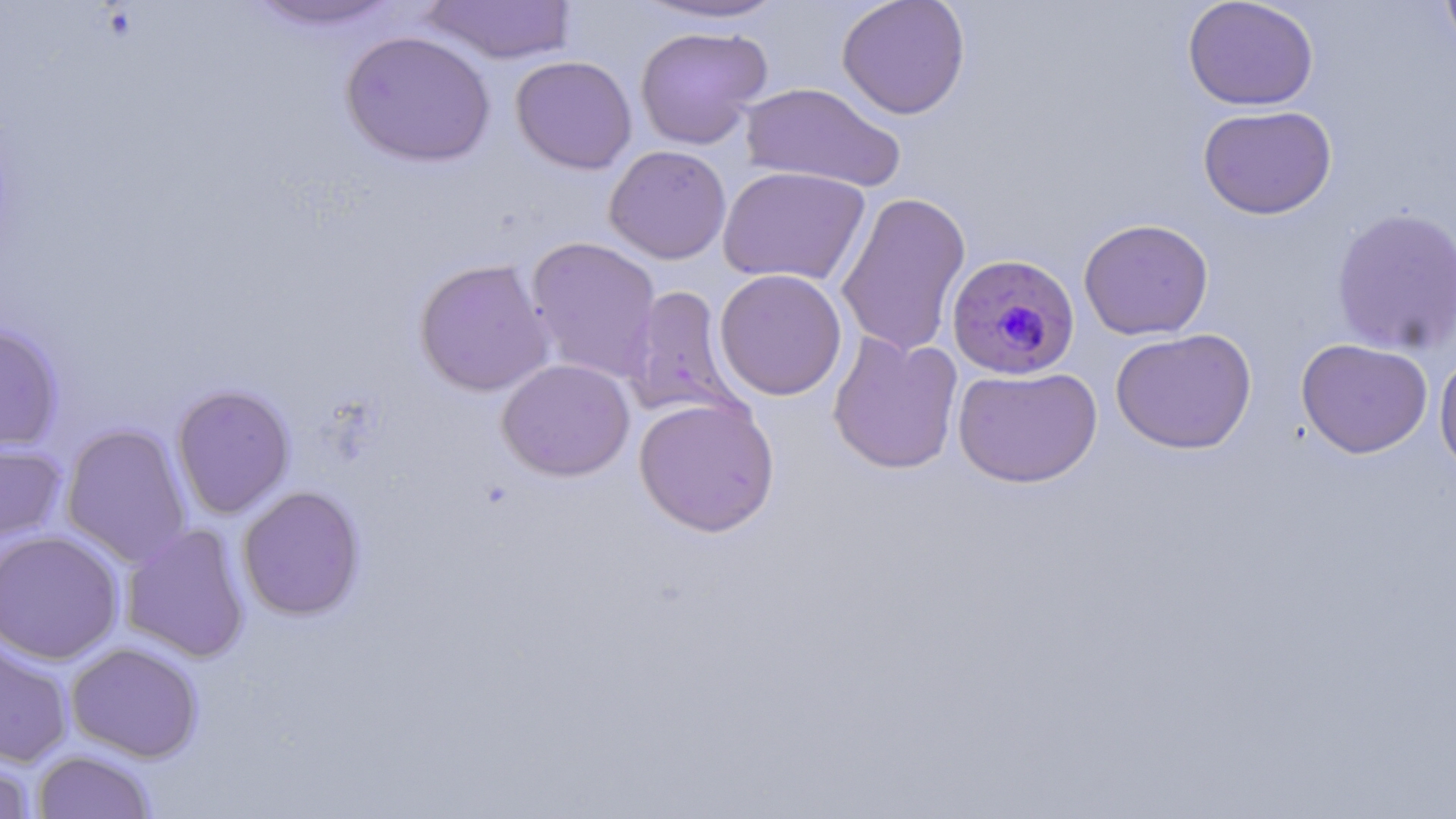
{
  "slide_level_diagnosis": "Plasmodium falciparum",
  "stain": "May-Grünwald-Giemsa",
  "modality": "optical microscopy",
  "field_of_view": "one of a larger specimen",
  "magnification": "1000x",
  "uninfected_red_blood_cell_locations": "approximate bounding boxes as (x1,y1)-(x2,y2) corner pairs in pixels: (243,0)-(406,33), (633,0)-(790,25), (836,0)-(971,119), (1182,0)-(1319,111), (1440,0)-(1456,55), (421,1)-(577,65), (634,25)-(772,149), (340,29)-(496,167), (511,55)-(637,174), (739,81)-(906,192), (1197,104)-(1337,220), (604,145)-(731,264), (718,165)-(871,287), (835,190)-(972,359), (1331,206)-(1456,355), (1078,218)-(1214,341), (525,236)-(662,384), (414,258)-(554,397), (714,269)-(847,401), (624,285)-(740,420), (0,322)-(64,453), (1110,328)-(1257,454), (827,332)-(963,475), (1295,338)-(1433,459), (1434,351)-(1456,477), (496,358)-(635,481), (952,365)-(1102,487), (171,384)-(295,519), (633,396)-(781,537), (60,423)-(192,568), (0,439)-(67,546), (237,485)-(365,621), (120,523)-(250,663), (0,529)-(124,665), (0,634)-(74,768), (65,642)-(203,762), (32,749)-(157,819), (0,754)-(38,819)",
  "plasmodium_falciparum_infected_red_blood_cell_locations": "approximate bounding boxes as (x1,y1)-(x2,y2) corner pairs in pixels: (947,253)-(1079,380)",
  "image_size": "1456×819 pixels",
  "preparation": "thin blood smear"
}